Point out each malaria parasite and classify it by life-cycle stage.
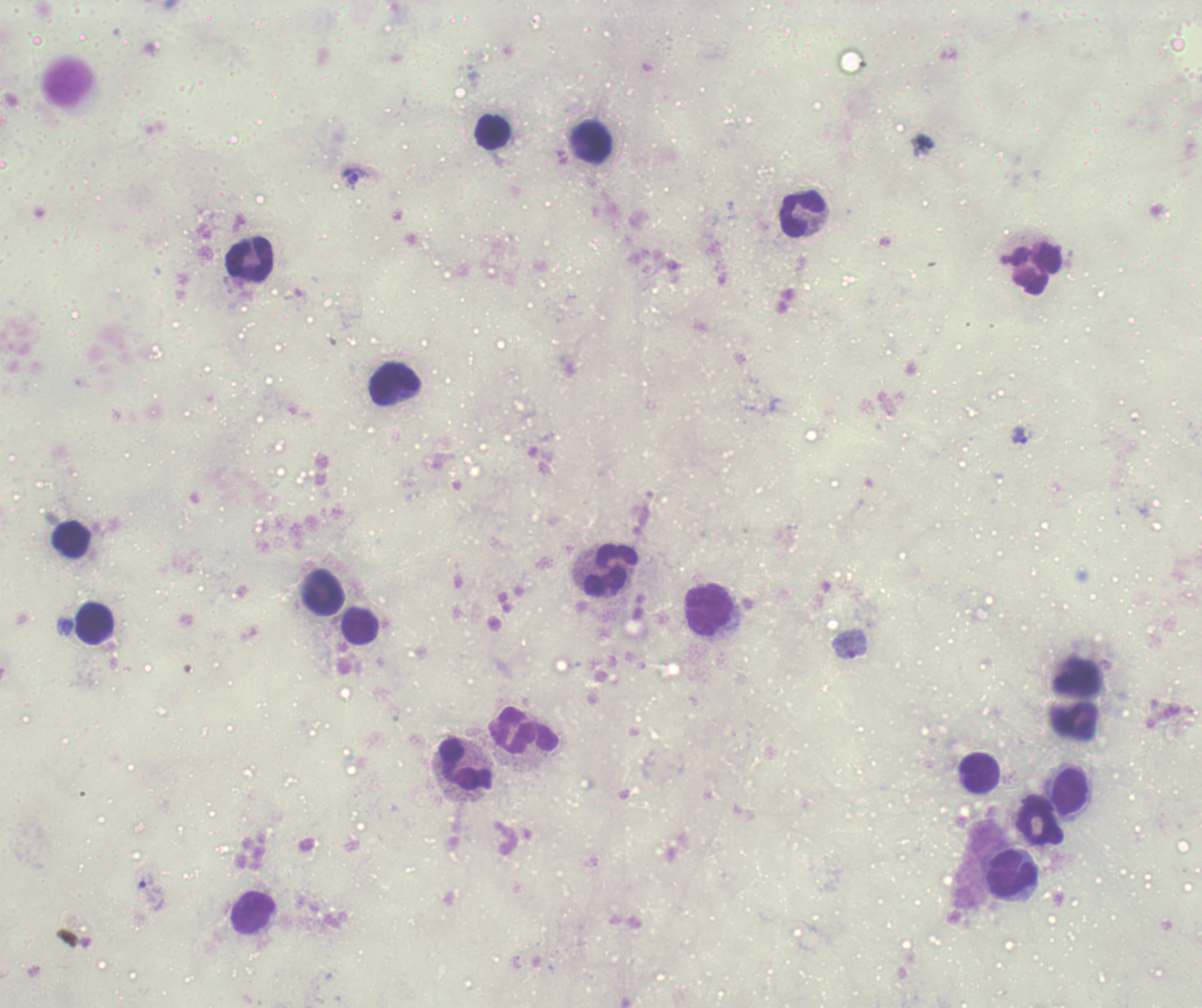
Approximate centers as (x, y) in pixels.
Trophozoites: (355, 177), (1020, 436), (850, 645), (146, 882).
No schizont or gametocyte forms observed.

Approximate centers as (x, y) in pixels. Leukocyte locations: (493, 133), (593, 142), (803, 216), (250, 259), (1038, 270), (396, 385), (71, 540), (612, 570), (323, 593), (710, 608), (96, 624), (360, 628), (524, 730), (467, 764), (979, 774), (1071, 791), (1040, 821), (1011, 875), (253, 912). Coloration quality: bad. Image is 1202×1008 pixels. Single field of view. Romanowsky-stained preparation. Thick blood film. Previously used in a real diagnosis. 100x magnification. Background quality: unsatisfactory.